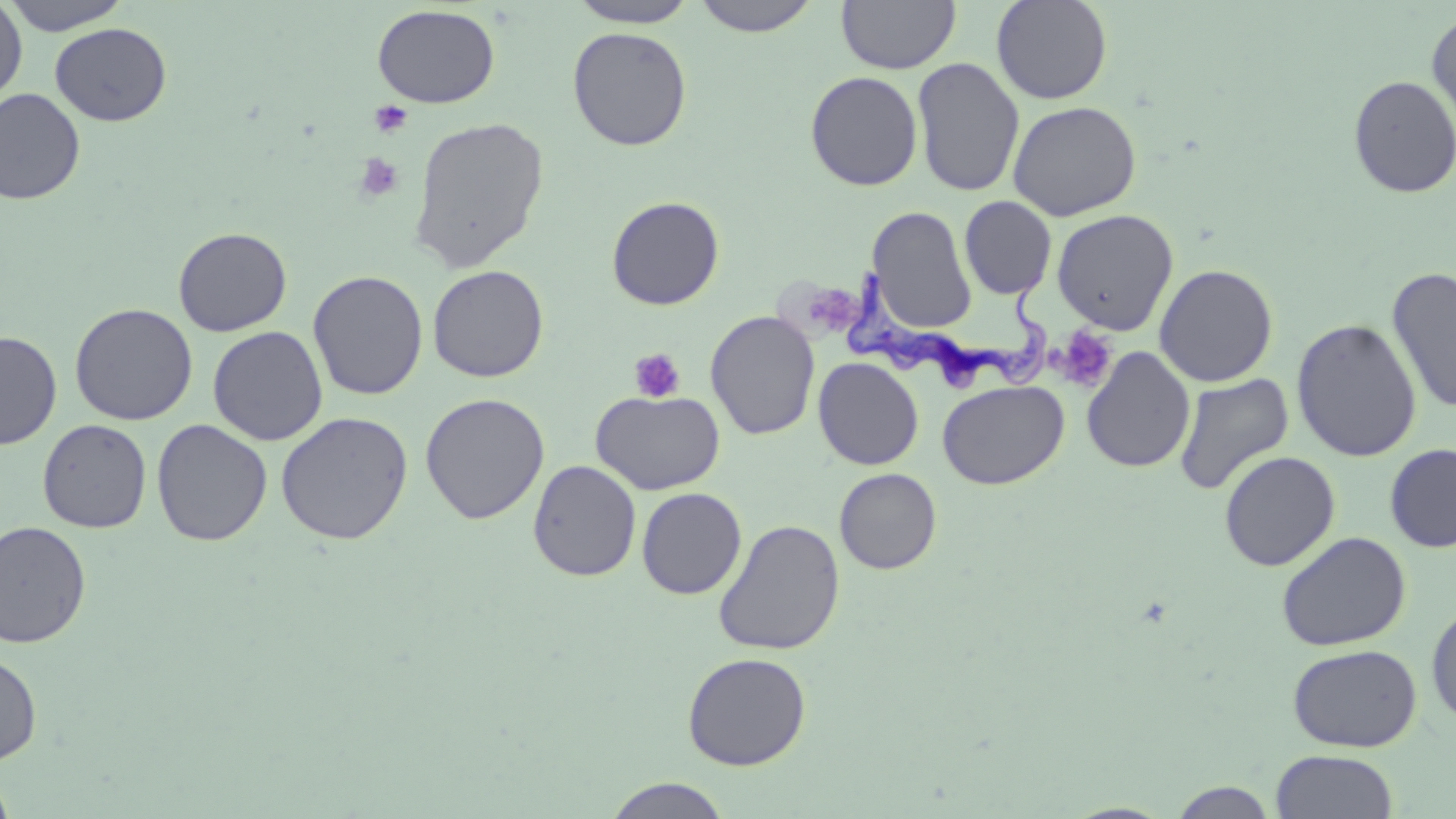 Approximate bounding boxes as [x1, y1, x2, y2] in pixels. Platelet locations: [369, 100, 413, 138], [354, 153, 404, 202], [810, 281, 863, 332], [1054, 326, 1118, 393], [628, 348, 686, 403]. Uninfected red blood cell locations: [3, 0, 132, 35], [566, 0, 700, 28], [689, 0, 825, 36], [836, 0, 960, 74], [991, 0, 1112, 104], [0, 1, 27, 106], [372, 4, 500, 109], [1426, 9, 1456, 135], [50, 23, 171, 126], [567, 26, 692, 151], [912, 57, 1025, 198], [805, 70, 923, 191], [1348, 75, 1456, 198], [0, 88, 86, 205], [1007, 100, 1142, 221], [407, 116, 549, 273], [606, 196, 725, 310], [959, 196, 1057, 300], [867, 205, 977, 333], [1051, 209, 1179, 335], [173, 227, 292, 336], [1154, 263, 1278, 387], [427, 264, 549, 382], [1387, 266, 1456, 415], [308, 269, 429, 400], [69, 303, 198, 425], [705, 310, 820, 440], [1291, 318, 1421, 462], [207, 326, 328, 445], [0, 330, 61, 450], [1081, 347, 1195, 473], [813, 357, 924, 470], [1173, 372, 1294, 495], [937, 380, 1069, 490], [590, 389, 726, 495], [420, 393, 550, 525], [275, 411, 414, 545], [151, 418, 272, 546], [37, 419, 152, 533], [1385, 444, 1456, 552], [1218, 451, 1341, 571], [528, 460, 642, 582], [834, 468, 941, 574], [636, 488, 746, 599], [712, 519, 845, 655], [0, 520, 92, 648], [1276, 531, 1411, 651], [1426, 602, 1456, 731], [1287, 643, 1422, 752], [0, 652, 42, 765], [682, 652, 811, 771], [1271, 749, 1399, 819], [0, 769, 17, 819], [605, 777, 731, 818], [1167, 780, 1280, 818]. Trypanosoma brucei locations: [845, 252, 1052, 392]. Slide-level diagnosis: Trypanosoma brucei. Captured at 1000x magnification. Single field of view. Optical microscopy. Thin blood smear. May-Grünwald-Giemsa-stained preparation. Image is 1456×819 pixels.